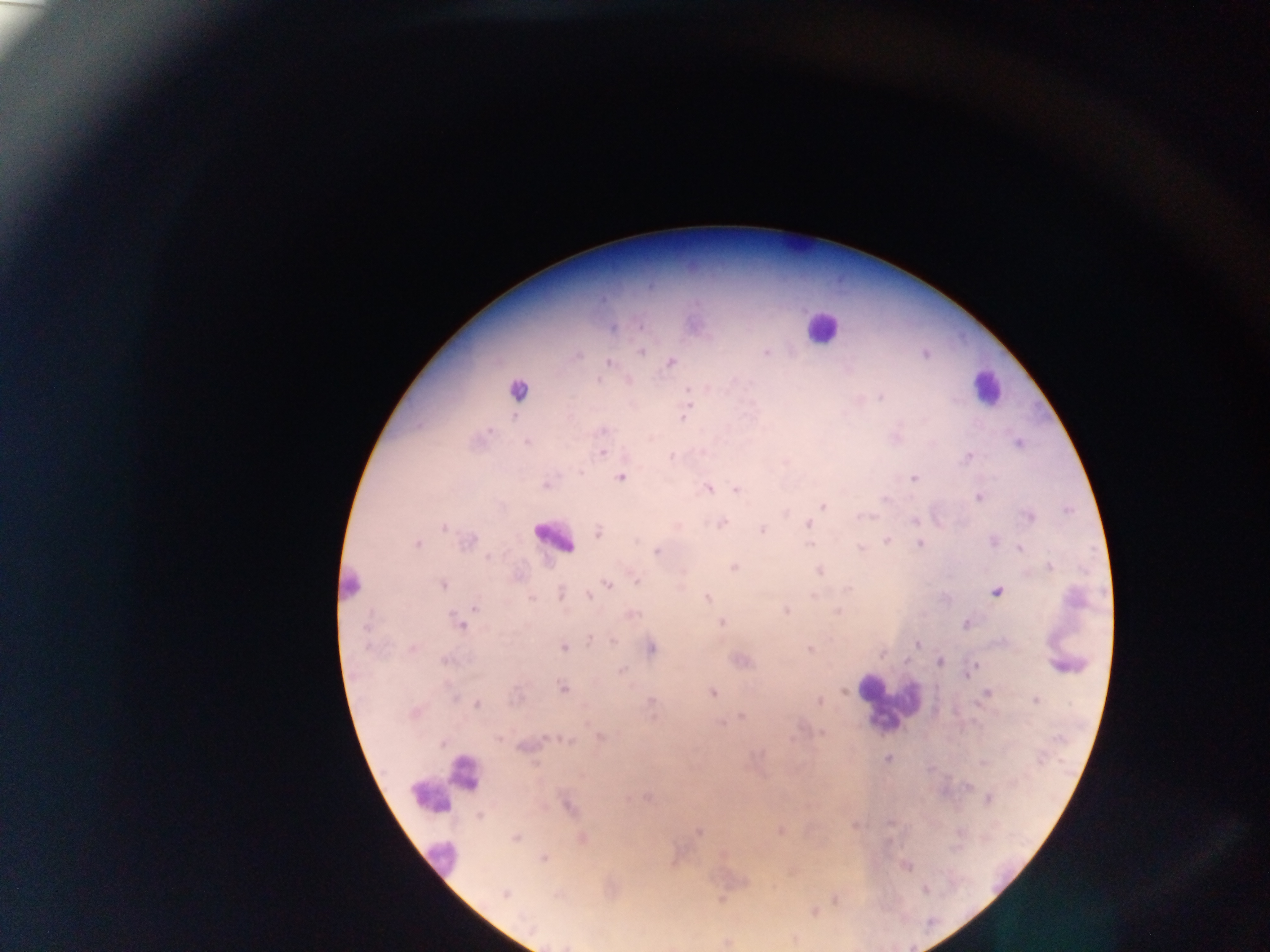
{
  "country": "Ghana",
  "leukocyte_locations": "approximate centers as {x, y} in pixels: {798, 241}, {820, 327}, {986, 388}, {553, 537}, {350, 586}, {1068, 664}, {885, 701}, {466, 773}, {448, 782}, {440, 857}",
  "image_size": "1270×952 pixels",
  "malaria_parasite_locations": "approximate centers as {x, y} in pixels: {694, 325}, {613, 326}, {641, 351}, {766, 352}, {576, 355}, {608, 362}, {670, 362}, {517, 391}, {683, 413}, {527, 441}, {1019, 442}, {602, 452}, {969, 455}, {671, 456}, {621, 477}, {915, 478}, {546, 484}, {708, 488}, {736, 489}, {980, 496}, {823, 505}, {1028, 516}, {915, 520}, {721, 523}, {809, 525}, {444, 526}, {763, 529}, {599, 532}, {887, 540}, {467, 541}, {994, 541}, {810, 543}, {920, 544}, {416, 545}, {1020, 547}, {860, 549}, {656, 551}, {1050, 566}, {733, 567}, {820, 570}, {636, 581}, {443, 583}, {607, 584}, {997, 591}, {560, 593}, {589, 596}, {814, 596}, {707, 598}, {475, 605}, {786, 611}, {838, 612}, {631, 614}, {459, 621}, {721, 622}, {965, 623}, {591, 638}, {917, 644}, {562, 646}, {412, 648}, {650, 648}, {810, 648}, {882, 652}, {445, 660}, {741, 661}, {939, 662}, {974, 666}, {621, 671}, {970, 671}, {563, 687}, {844, 691}, {711, 692}, {987, 693}, {1036, 700}, {819, 701}, {650, 702}, {476, 704}, {414, 712}, {742, 716}, {722, 723}, {821, 734}, {600, 737}, {526, 745}, {887, 757}, {988, 798}, {567, 805}, {854, 824}, {780, 830}, {699, 831}, {515, 837}, {583, 838}, {543, 857}, {905, 866}, {792, 869}, {504, 893}, {720, 898}, {837, 898}, {812, 911}, {795, 938}, {726, 941}",
  "field_of_view": "single",
  "capture": "mobile-phone photograph through a microscope",
  "preparation": "thick blood smear"
}